Identify the preparation type.
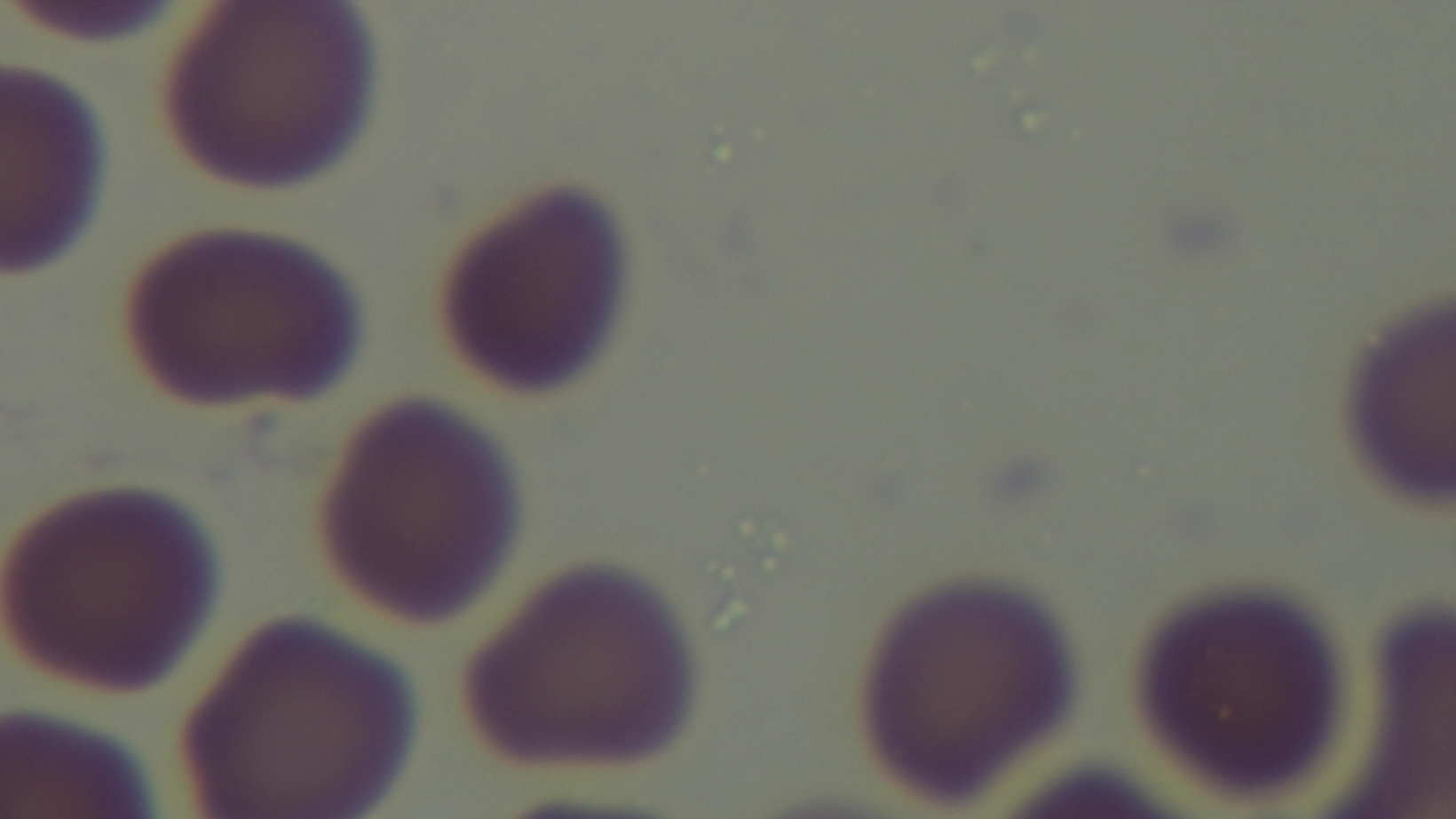
A thin smear.

Summary:
  - Modality: light microscopy
  - Capture: mounted 4K digital camera
  - Field of view: single
  - Stain: Giemsa
  - Malaria status: negative
  - Objective: 100x oil immersion